Comment on the morphology of the red blood cells.
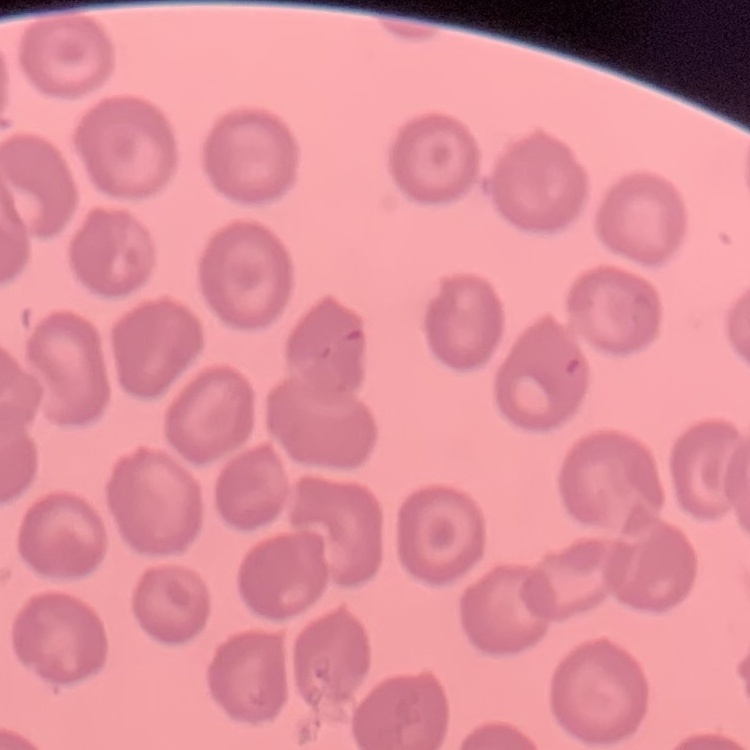
They show no rouleaux formation.

image_type: square crop of a larger photomicrograph
preparation: thin blood film
stain: Field's or Giemsa